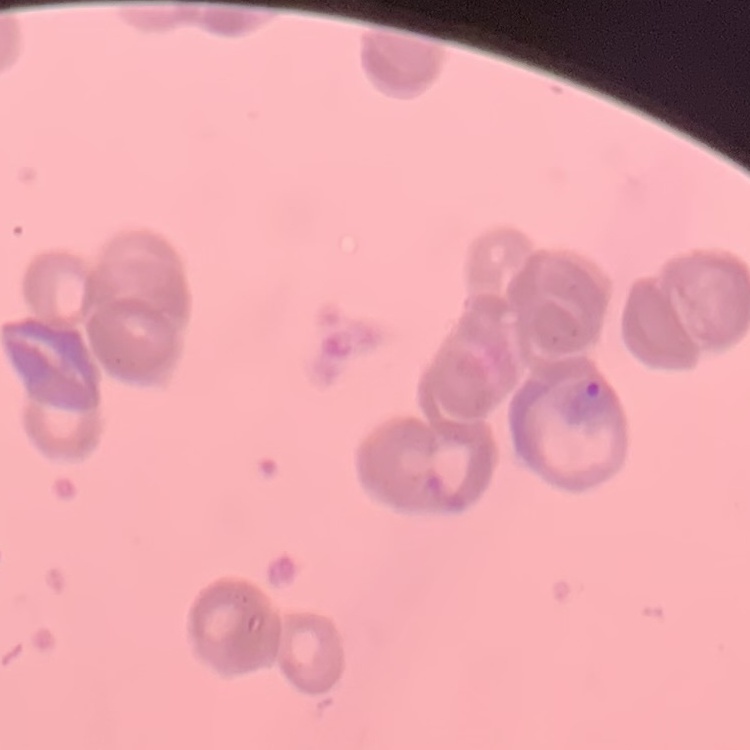
red blood cell morphology = rouleaux formation
stain = Field's or Giemsa
preparation = thin blood smear
image type = square crop of a larger photomicrograph